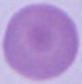
Summary:
  - Identification: red blood cell
  - Modality: micrograph
  - Magnification: 1000x